Assess this cell for malaria.
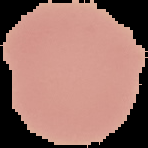
It is uninfected.

{
  "image_type": "segmented cell region on a black background",
  "image_size": "148×148 pixels",
  "preparation": "thin blood smear"
}